State which parasite is depicted.
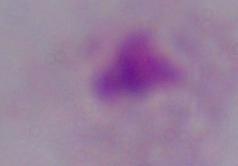
This is a trichomonad.

modality = micrograph
magnification = 1000x